Locate every blood parasite and identify its species.
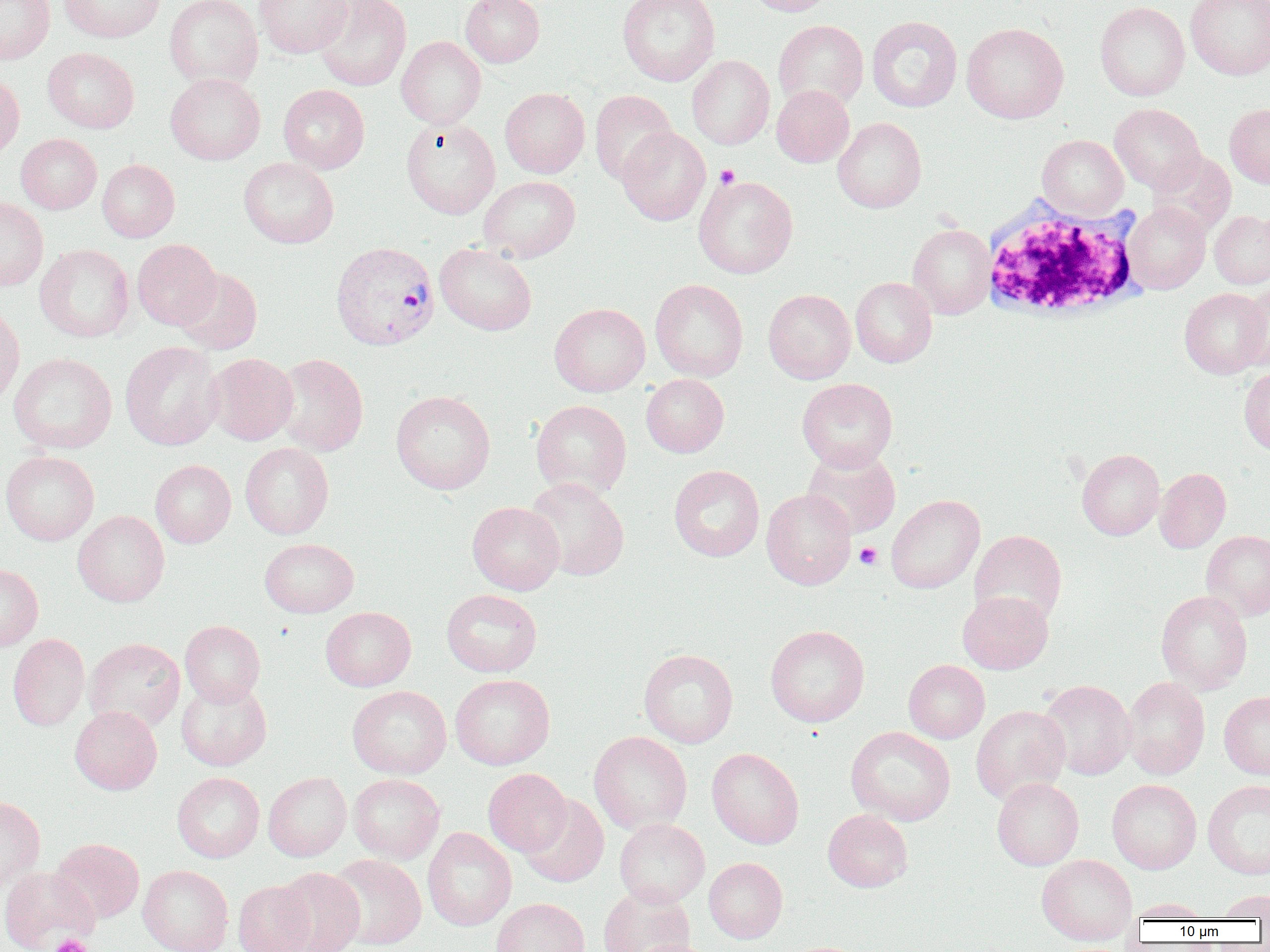

Approximate bounding boxes as named x1/y1/x2/y2 corners in pixels.
Plasmodium vivax-infected red blood cells: (x1=330, y1=241, x2=440, y2=351).
No Plasmodium falciparum, Plasmodium ovale, Plasmodium malariae, Babesia divergens, or Trypanosoma brucei observed.

Summary:
  - Uninfected red blood cell locations: (x1=0, y1=0, x2=55, y2=64), (x1=59, y1=0, x2=165, y2=43), (x1=164, y1=0, x2=263, y2=90), (x1=253, y1=0, x2=353, y2=58), (x1=312, y1=0, x2=411, y2=91), (x1=460, y1=0, x2=545, y2=67), (x1=618, y1=0, x2=720, y2=86), (x1=745, y1=0, x2=835, y2=16), (x1=1185, y1=0, x2=1270, y2=80), (x1=1095, y1=1, x2=1190, y2=101), (x1=867, y1=16, x2=962, y2=112), (x1=773, y1=20, x2=868, y2=111), (x1=961, y1=22, x2=1069, y2=123), (x1=396, y1=36, x2=486, y2=128), (x1=43, y1=47, x2=139, y2=133), (x1=687, y1=55, x2=774, y2=149), (x1=0, y1=73, x2=24, y2=164), (x1=165, y1=73, x2=265, y2=165), (x1=279, y1=84, x2=369, y2=173), (x1=771, y1=85, x2=854, y2=167), (x1=500, y1=87, x2=589, y2=178), (x1=589, y1=90, x2=677, y2=185), (x1=1109, y1=104, x2=1205, y2=194), (x1=1225, y1=104, x2=1270, y2=188), (x1=401, y1=118, x2=500, y2=218), (x1=833, y1=118, x2=926, y2=212), (x1=617, y1=127, x2=710, y2=225), (x1=15, y1=134, x2=102, y2=214), (x1=1037, y1=135, x2=1129, y2=220), (x1=1149, y1=151, x2=1236, y2=237), (x1=239, y1=157, x2=339, y2=248), (x1=97, y1=159, x2=180, y2=242), (x1=479, y1=175, x2=580, y2=263), (x1=693, y1=175, x2=797, y2=278), (x1=0, y1=197, x2=48, y2=291), (x1=1123, y1=202, x2=1210, y2=294), (x1=1209, y1=210, x2=1270, y2=289), (x1=908, y1=224, x2=995, y2=319), (x1=131, y1=239, x2=221, y2=330), (x1=435, y1=243, x2=537, y2=336), (x1=35, y1=244, x2=134, y2=342), (x1=175, y1=269, x2=262, y2=354), (x1=850, y1=277, x2=937, y2=367), (x1=650, y1=279, x2=748, y2=382), (x1=1237, y1=281, x2=1270, y2=371), (x1=1179, y1=287, x2=1269, y2=379), (x1=763, y1=289, x2=855, y2=384), (x1=0, y1=303, x2=24, y2=408), (x1=549, y1=303, x2=650, y2=396), (x1=120, y1=341, x2=223, y2=450), (x1=9, y1=352, x2=117, y2=454), (x1=206, y1=353, x2=298, y2=445), (x1=272, y1=353, x2=368, y2=456), (x1=1239, y1=366, x2=1270, y2=455), (x1=641, y1=374, x2=729, y2=457), (x1=797, y1=378, x2=898, y2=472), (x1=391, y1=390, x2=495, y2=494), (x1=531, y1=399, x2=632, y2=499), (x1=240, y1=443, x2=334, y2=538), (x1=802, y1=448, x2=901, y2=539), (x1=1077, y1=449, x2=1165, y2=540), (x1=0, y1=450, x2=99, y2=545), (x1=150, y1=460, x2=236, y2=548), (x1=669, y1=464, x2=765, y2=562), (x1=1154, y1=467, x2=1231, y2=553), (x1=524, y1=477, x2=629, y2=581), (x1=761, y1=489, x2=856, y2=590), (x1=885, y1=495, x2=984, y2=594), (x1=467, y1=502, x2=565, y2=595), (x1=72, y1=510, x2=170, y2=607), (x1=969, y1=530, x2=1067, y2=625), (x1=1201, y1=530, x2=1270, y2=621), (x1=259, y1=538, x2=358, y2=617), (x1=0, y1=564, x2=43, y2=651), (x1=441, y1=589, x2=542, y2=677), (x1=957, y1=590, x2=1053, y2=674), (x1=1156, y1=590, x2=1253, y2=694), (x1=320, y1=606, x2=416, y2=691), (x1=180, y1=620, x2=265, y2=707), (x1=765, y1=625, x2=869, y2=727), (x1=8, y1=634, x2=90, y2=731), (x1=84, y1=638, x2=185, y2=732), (x1=639, y1=649, x2=738, y2=748), (x1=903, y1=660, x2=990, y2=743), (x1=450, y1=674, x2=555, y2=770), (x1=1121, y1=676, x2=1211, y2=779), (x1=176, y1=679, x2=272, y2=770), (x1=1038, y1=680, x2=1136, y2=780), (x1=347, y1=685, x2=452, y2=779), (x1=1219, y1=690, x2=1270, y2=780), (x1=70, y1=705, x2=162, y2=794), (x1=971, y1=705, x2=1071, y2=804), (x1=846, y1=726, x2=956, y2=826), (x1=589, y1=731, x2=692, y2=834), (x1=707, y1=747, x2=804, y2=849), (x1=483, y1=768, x2=571, y2=857), (x1=263, y1=771, x2=352, y2=861), (x1=172, y1=772, x2=264, y2=862), (x1=348, y1=773, x2=445, y2=864), (x1=992, y1=777, x2=1084, y2=870), (x1=1107, y1=779, x2=1201, y2=874), (x1=1202, y1=779, x2=1270, y2=880), (x1=519, y1=794, x2=609, y2=887), (x1=0, y1=796, x2=45, y2=890), (x1=823, y1=809, x2=913, y2=892), (x1=614, y1=818, x2=710, y2=907), (x1=422, y1=827, x2=516, y2=931), (x1=50, y1=838, x2=144, y2=923), (x1=327, y1=853, x2=426, y2=950), (x1=1036, y1=854, x2=1137, y2=944), (x1=704, y1=857, x2=787, y2=943), (x1=138, y1=865, x2=233, y2=952), (x1=0, y1=866, x2=97, y2=951), (x1=274, y1=867, x2=365, y2=952), (x1=233, y1=880, x2=315, y2=952), (x1=598, y1=886, x2=695, y2=952), (x1=1214, y1=890, x2=1270, y2=920), (x1=491, y1=898, x2=589, y2=952), (x1=1125, y1=899, x2=1214, y2=921), (x1=634, y1=938, x2=714, y2=952)
  - Platelet locations: (x1=715, y1=164, x2=739, y2=188), (x1=855, y1=542, x2=882, y2=569), (x1=50, y1=934, x2=93, y2=952)
  - White blood cell locations: (x1=979, y1=196, x2=1145, y2=324)
  - Slide-level diagnosis: Plasmodium vivax
  - Preparation: thin blood film
  - Modality: optical microscopy
  - Image size: 1270×952 pixels
  - Field of view: single
  - Magnification: 1000x